Describe the morphology of the red blood cells.
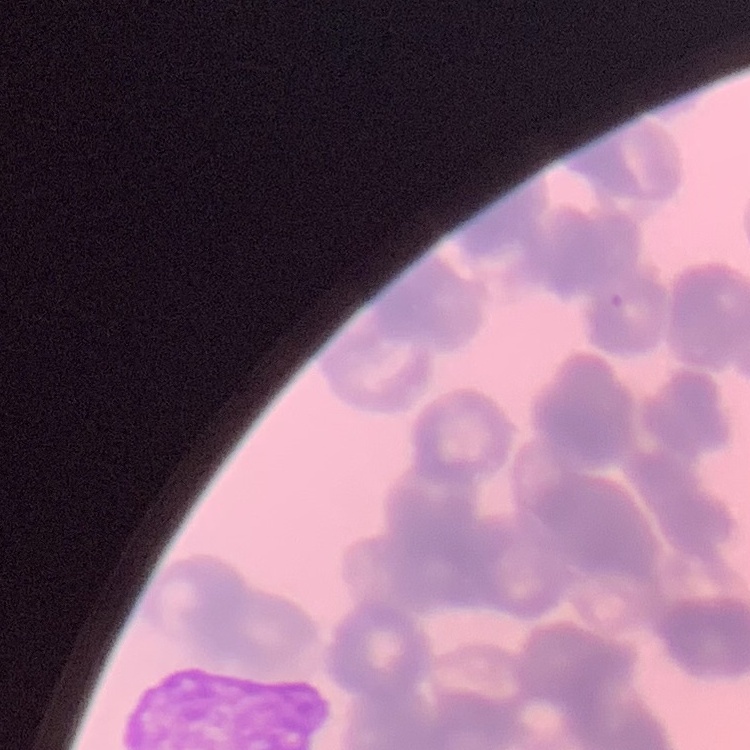
They show rouleaux formation.

image type = one tile cut from a larger photomicrograph
stain = Field's or Giemsa
preparation = thin blood smear